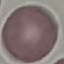

result: no malaria parasites detected
preparation: thin smear
capture: smartphone camera at the microscope eyepiece
stain: Giemsa
image_type: automatically extracted cell patch, resized to 64 × 64 pixels